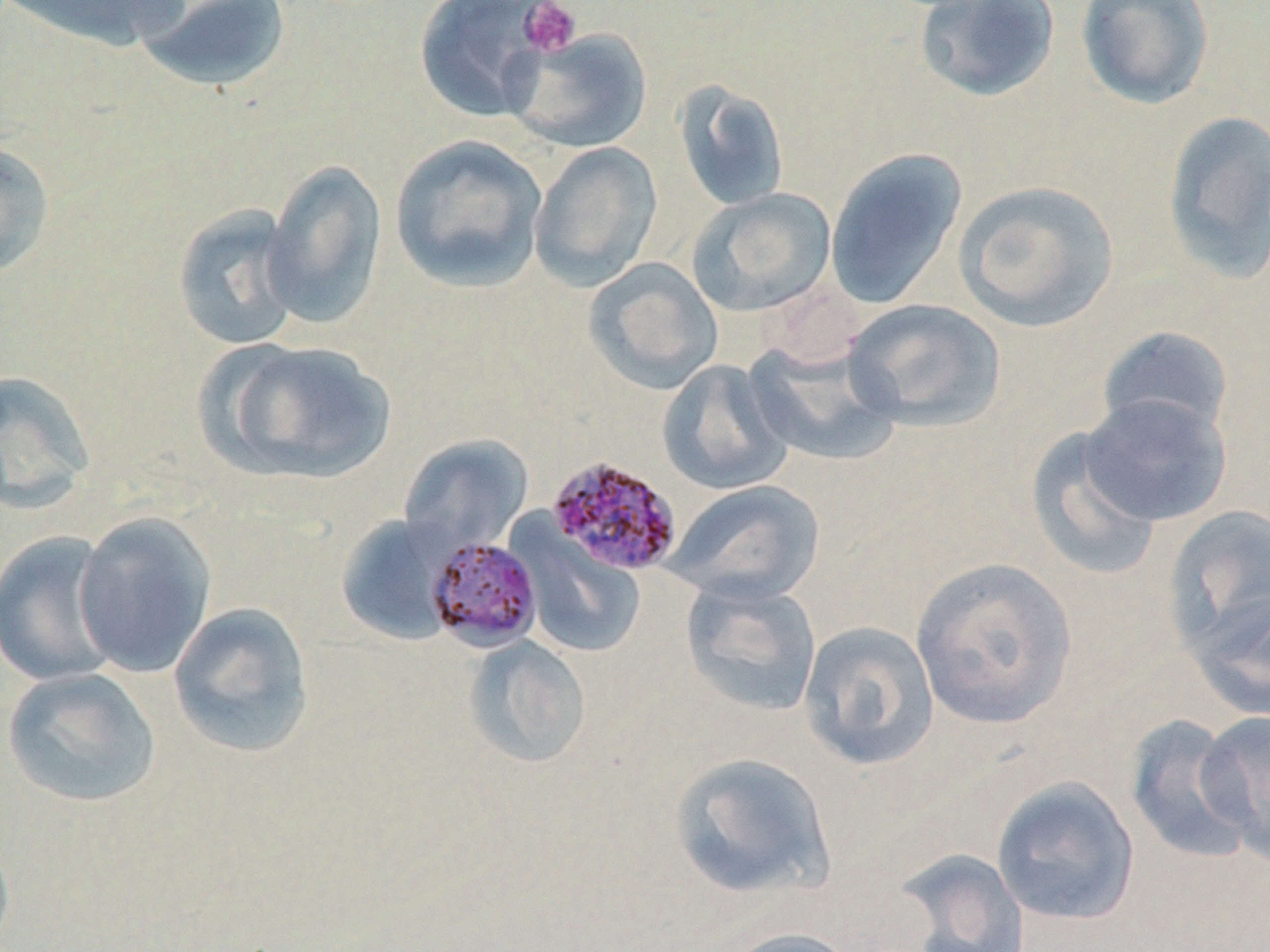
{
  "slide_level_diagnosis": "Plasmodium malariae",
  "preparation": "thin blood smear",
  "image_size": "1270×952 pixels",
  "platelet_locations": "approximate bounding boxes as (x1,y1)-(x2,y2) corner pairs in pixels: (518,1)-(583,57)",
  "field_of_view": "one of a larger specimen",
  "plasmodium_malariae_infected_red_blood_cell_locations": "approximate bounding boxes as (x1,y1)-(x2,y2) corner pairs in pixels: (545,454)-(684,577), (424,536)-(542,653)",
  "modality": "light microscopy",
  "stain": "May-Grünwald-Giemsa",
  "uninfected_red_blood_cell_locations": "approximate bounding boxes as (x1,y1)-(x2,y2) corner pairs in pixels: (3,0)-(192,54), (132,0)-(294,93), (413,0)-(554,123), (913,0)-(1061,103), (1076,0)-(1215,110), (505,28)-(653,153), (673,81)-(790,212), (1161,110)-(1270,284), (390,133)-(549,293), (0,138)-(56,280), (528,142)-(663,291), (825,146)-(968,310), (262,159)-(387,331), (954,180)-(1120,332), (688,188)-(836,317), (172,204)-(305,351), (584,257)-(724,395), (844,299)-(1007,432), (1097,326)-(1235,442), (204,338)-(397,486), (744,338)-(902,467), (657,358)-(793,495), (0,370)-(97,515), (1077,392)-(1231,527), (1025,427)-(1163,581), (398,434)-(533,556), (666,479)-(826,605), (1163,504)-(1270,659), (72,510)-(217,679), (335,513)-(458,645), (512,524)-(648,658), (0,528)-(123,687), (909,556)-(1078,729), (680,575)-(822,717), (1187,588)-(1270,723), (167,601)-(316,759), (797,620)-(940,771), (462,635)-(592,769), (2,667)-(161,809), (1196,711)-(1269,862), (1125,713)-(1256,865), (667,751)-(836,900), (991,776)-(1141,926), (893,847)-(1031,952), (721,927)-(859,952)",
  "magnification": "1000x"
}